Classify this cell by malaria status.
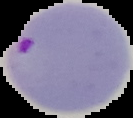

It is parasitized.

image type = segmented cell region with the area outside set to black
image size = 133×118 pixels
preparation = thin blood smear